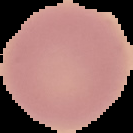
From a thin blood smear. The area outside the segmented cell region is set to black. Malaria status: uninfected. Image is 133×133 pixels.